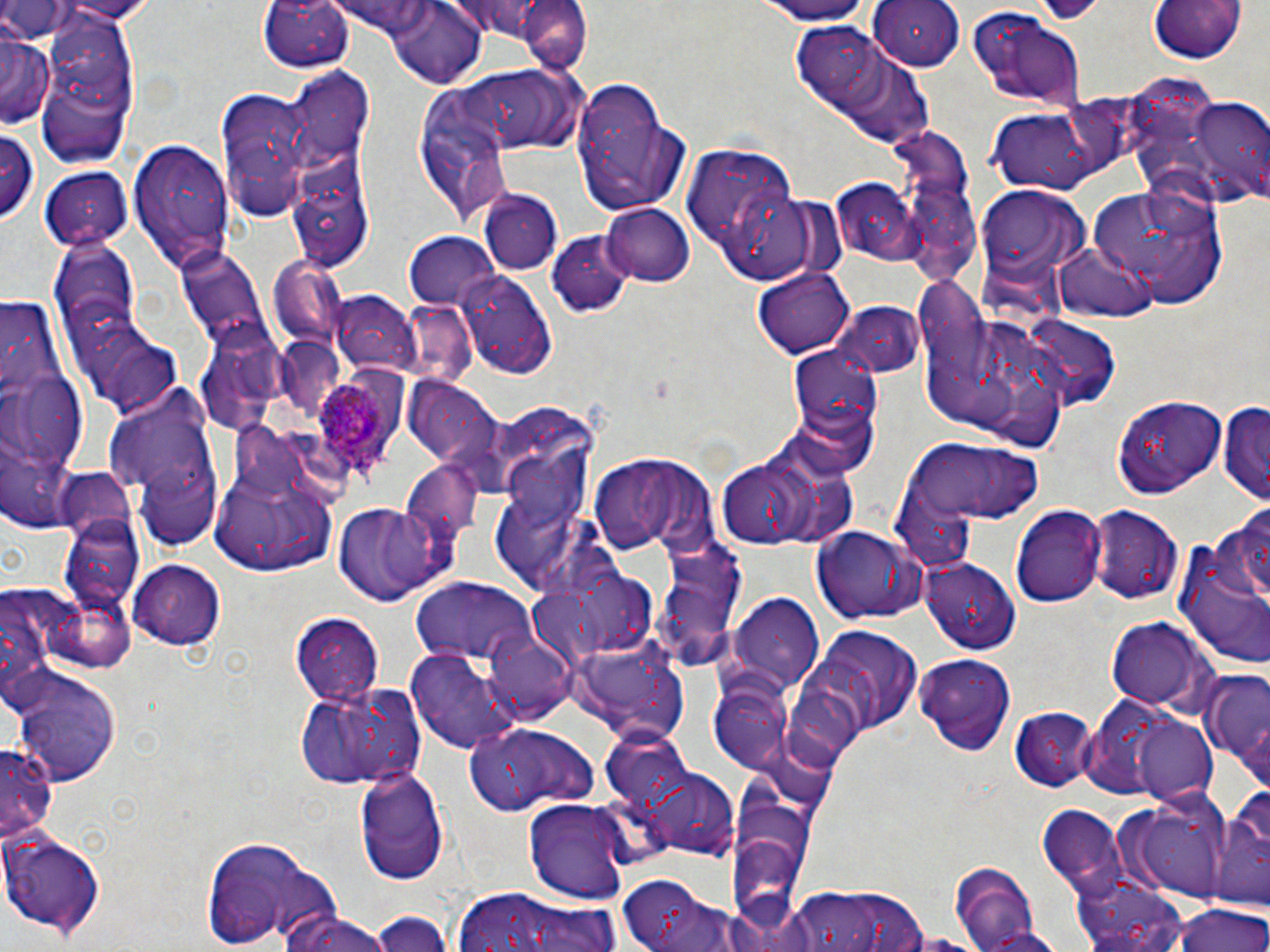

Summary:
  - Coordinate format: approximate bounding boxes as (x1,y1)-(x2,y2) corner pairs in pixels
  - Uninfected red blood cell locations: (0,0)-(83,41), (48,0)-(159,20), (257,0)-(353,74), (517,0)-(590,75), (749,0)-(881,24), (1145,0)-(1251,64), (866,1)-(967,72), (383,3)-(489,89), (32,9)-(146,171), (966,9)-(1088,110), (789,22)-(932,149), (2,28)-(53,129), (453,67)-(587,153), (285,69)-(374,176), (572,76)-(686,216), (219,84)-(316,217), (412,92)-(512,227), (1187,99)-(1270,201), (991,109)-(1095,193), (0,125)-(40,225), (891,134)-(981,282), (130,141)-(232,277), (681,141)-(801,263), (284,153)-(375,271), (40,165)-(133,249), (1084,178)-(1230,307), (829,179)-(917,265), (978,186)-(1085,278), (478,191)-(561,277), (602,202)-(696,286), (405,232)-(500,311), (549,233)-(635,318), (1055,242)-(1155,323), (177,248)-(272,350), (266,257)-(350,347), (754,266)-(855,356), (458,267)-(560,382), (331,289)-(420,377), (834,301)-(924,377), (211,326)-(305,407), (276,334)-(338,408), (786,341)-(886,470), (1,369)-(90,481), (103,375)-(220,537), (405,378)-(503,472), (1116,393)-(1225,496), (1220,402)-(1270,506), (904,436)-(1047,532), (589,454)-(717,553), (710,456)-(824,551), (209,461)-(342,577), (137,462)-(223,551), (405,464)-(486,553), (330,501)-(452,605), (1010,503)-(1104,608), (1091,505)-(1183,606), (59,513)-(143,610), (1171,516)-(1269,670), (810,525)-(929,624), (652,535)-(747,667), (923,558)-(1022,653), (128,559)-(227,650), (413,580)-(537,669), (731,595)-(824,691), (292,612)-(385,704), (1102,616)-(1218,714), (799,625)-(922,745), (484,630)-(578,722), (563,633)-(686,745), (409,650)-(520,754), (914,652)-(1018,754), (8,668)-(122,785), (1201,670)-(1270,771), (708,681)-(797,775), (297,682)-(426,789), (1075,693)-(1203,801), (1010,706)-(1099,792), (1134,717)-(1219,805), (464,723)-(599,816), (600,731)-(692,815), (0,744)-(56,841), (356,765)-(451,885), (643,770)-(738,860), (1210,788)-(1269,911), (1113,791)-(1234,904), (525,799)-(630,906), (1038,805)-(1128,895), (726,812)-(814,929), (2,824)-(106,937), (195,836)-(340,951), (948,861)-(1048,952), (617,875)-(723,952), (1069,877)-(1191,952), (788,882)-(929,952), (446,892)-(620,952), (1168,902)-(1270,952), (371,908)-(454,951), (277,913)-(388,952), (971,926)-(1076,952)
  - Plasmodium ovale-infected red blood cell locations: (309,379)-(400,490)
  - Slide-level diagnosis: Plasmodium ovale
  - Preparation: thin blood smear
  - Stain: May-Grünwald-Giemsa
  - Modality: light microscopy
  - Image size: 1270×952 pixels
  - Field of view: single
  - Magnification: 1000x